Identify the cell.
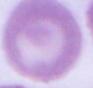

An erythrocyte.

modality = micrograph
magnification = 1000x